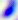
Toxoplasma gondii is seen. Micrograph. 400x magnification.